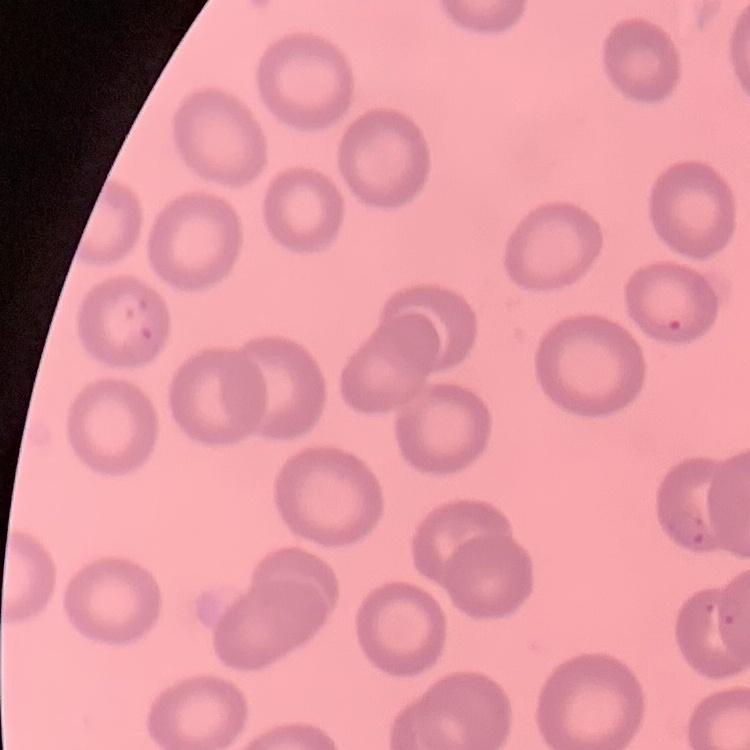
erythrocyte morphology = no rouleaux formation
preparation = thin blood film
stain = Field's or Giemsa
image type = one tile cut from a larger photomicrograph